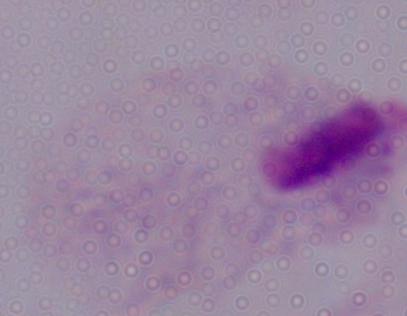
Summary:
  - Magnification: 1000x
  - Modality: photomicrograph
  - Identification: trichomonad